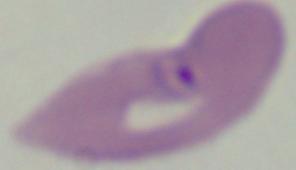

modality: photomicrograph
magnification: 1000x
identification: Babesia